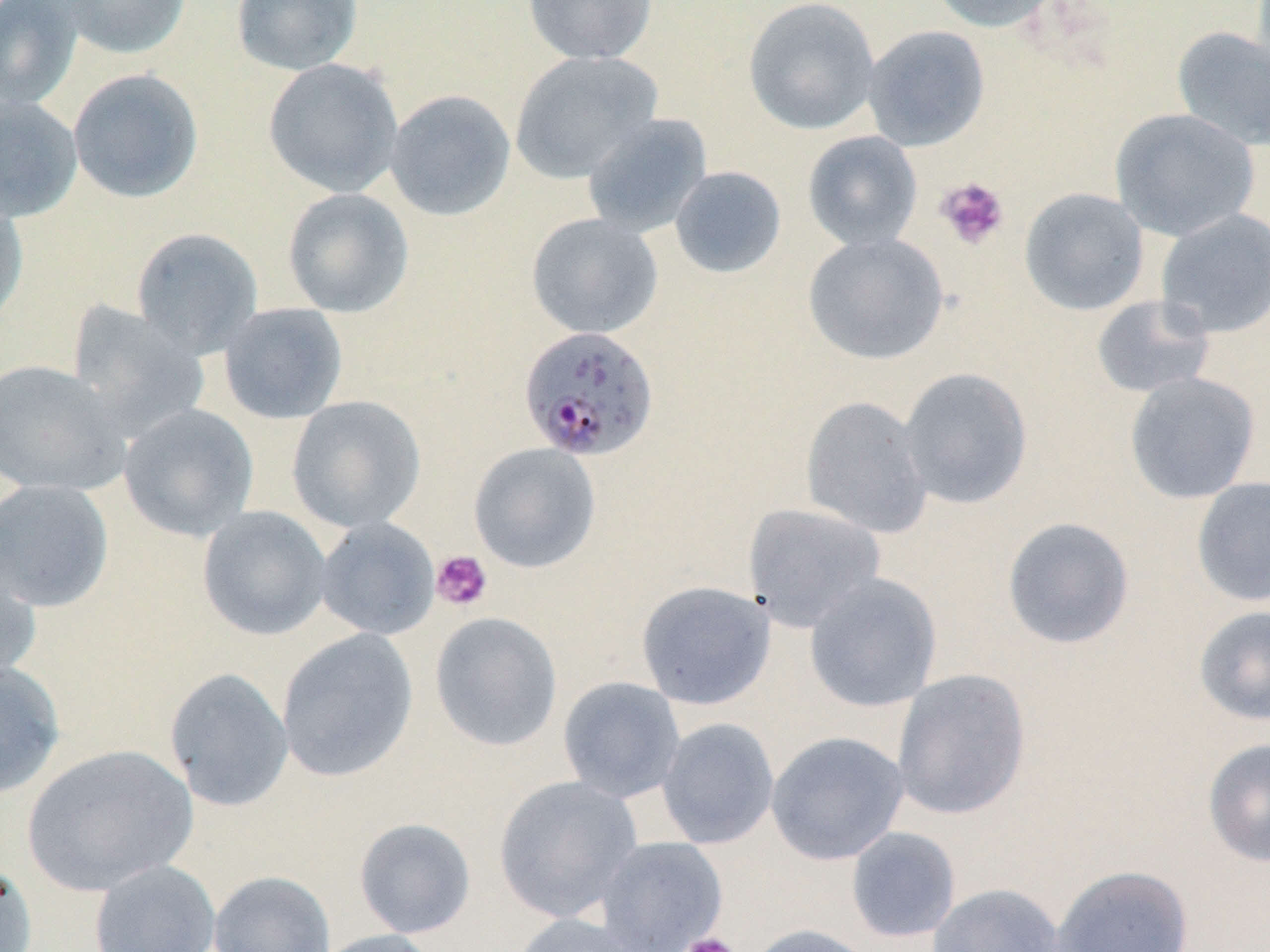

Summary:
  - Coordinate format: approximate bounding boxes as [x1, y1, x2, y2] in pixels
  - Uninfected red blood cell locations: [0, 0, 85, 111], [57, 0, 192, 60], [230, 0, 364, 75], [523, 0, 658, 65], [743, 0, 881, 136], [928, 0, 1062, 33], [862, 25, 990, 151], [1172, 26, 1270, 152], [509, 50, 662, 184], [263, 58, 403, 198], [67, 68, 204, 204], [385, 89, 516, 221], [0, 95, 83, 222], [1110, 108, 1260, 241], [580, 113, 712, 238], [802, 131, 923, 252], [669, 166, 787, 279], [282, 187, 414, 318], [1019, 187, 1149, 315], [0, 190, 30, 331], [1155, 208, 1270, 338], [525, 212, 663, 339], [131, 227, 263, 359], [803, 232, 949, 365], [1091, 295, 1215, 399], [66, 302, 211, 443], [218, 302, 349, 425], [0, 359, 131, 496], [898, 366, 1033, 509], [1124, 372, 1262, 505], [286, 395, 426, 534], [800, 396, 934, 538], [118, 403, 259, 542], [468, 443, 601, 573], [1191, 477, 1270, 607], [0, 479, 115, 613], [743, 502, 886, 633], [197, 506, 332, 641], [1001, 516, 1134, 649], [314, 517, 440, 640], [0, 550, 42, 685], [804, 573, 942, 713], [635, 580, 776, 710], [1193, 604, 1270, 727], [429, 611, 563, 752], [276, 628, 419, 782], [0, 659, 66, 799], [164, 667, 294, 812], [891, 668, 1031, 820], [557, 676, 685, 803], [657, 717, 779, 850], [766, 731, 909, 865], [1202, 737, 1270, 868], [21, 744, 198, 897], [492, 775, 643, 923], [353, 817, 477, 939], [845, 827, 961, 943], [594, 836, 728, 952], [0, 856, 38, 952], [89, 859, 221, 952], [1051, 864, 1194, 952], [208, 870, 336, 952], [928, 883, 1066, 952], [506, 912, 651, 952], [745, 923, 879, 952], [310, 929, 445, 952]
  - Platelet locations: [935, 176, 1010, 250], [431, 550, 493, 612], [678, 932, 741, 952]
  - Plasmodium falciparum-infected red blood cell locations: [518, 326, 659, 462]
  - Slide-level diagnosis: Plasmodium falciparum
  - Preparation: thin blood film
  - Image size: 1270×952 pixels
  - Stain: May-Grünwald-Giemsa
  - Field of view: one of a larger specimen
  - Magnification: 1000x
  - Modality: light microscopy